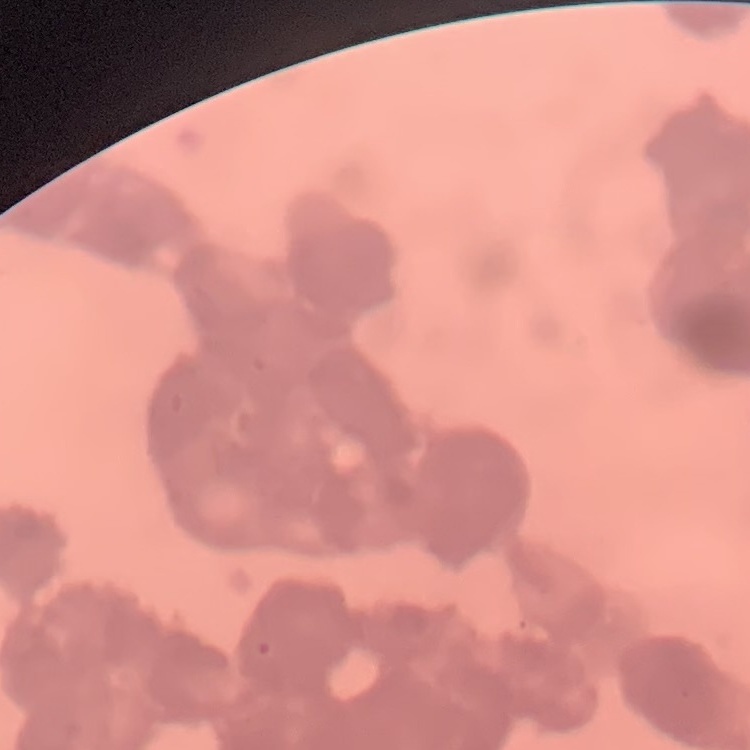 The erythrocytes show rouleaux formation. Thin blood smear. Square crop of a larger photomicrograph. Stained with either Field's or Giemsa.